Classify this cell by malaria status.
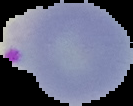

It is parasitized.

image type = segmented cell region with the area outside set to black
image size = 133×106 pixels
preparation = thin blood film